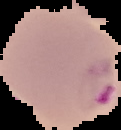
image size = 121×130 pixels
preparation = thin blood film
malaria status = parasitized
image type = segmented cell region with the area outside set to black